Find each parasitized RBC.
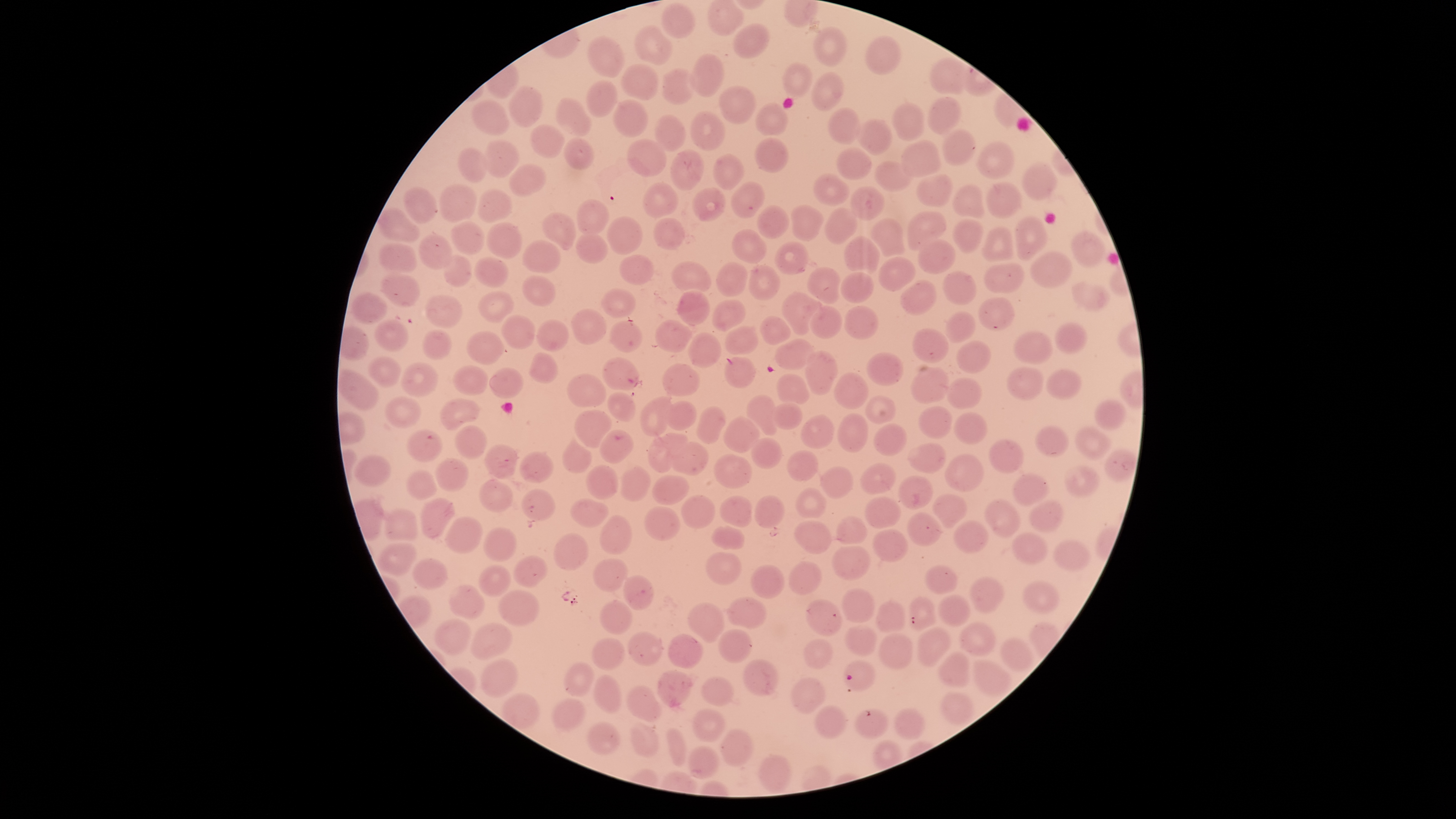

Approximate bounding boxes as {left, top, right, bottom} in pixels.
Parasitized RBCs: {843, 661, 877, 690}.

Approximate bounding boxes as {left, top, right, bottom} in pixels.
Summary:
  - Uninfected RBCs: {707, 0, 746, 36}, {661, 4, 697, 38}, {733, 23, 770, 58}, {634, 26, 673, 65}, {813, 27, 848, 66}, {865, 35, 901, 76}, {588, 37, 624, 78}, {690, 53, 725, 96}, {929, 56, 969, 95}, {783, 62, 813, 97}, {620, 63, 658, 100}, {662, 68, 694, 105}, {812, 73, 845, 111}, {586, 81, 618, 118}, {509, 86, 545, 128}, {718, 86, 756, 125}, {927, 97, 962, 134}, {555, 98, 591, 135}, {613, 100, 648, 137}, {470, 102, 509, 135}, {891, 103, 924, 141}, {755, 104, 790, 136}, {828, 107, 860, 145}, {689, 110, 726, 151}, {655, 115, 686, 150}, {858, 119, 892, 156}, {530, 124, 564, 159}, {941, 129, 976, 166}, {564, 138, 593, 169}, {627, 138, 666, 177}, {754, 138, 787, 173}, {484, 140, 519, 177}, {901, 140, 941, 177}, {977, 142, 1014, 178}, {836, 147, 872, 180}, {458, 148, 489, 183}, {671, 149, 704, 191}, {713, 153, 743, 192}, {875, 160, 914, 191}, {510, 163, 545, 197}, {1022, 164, 1058, 200}, {813, 173, 850, 208}, {917, 174, 953, 207}, {643, 182, 679, 217}, {731, 182, 765, 219}, {986, 182, 1023, 219}, {440, 184, 477, 223}, {952, 184, 985, 219}, {849, 186, 886, 220}, {403, 187, 438, 223}, {692, 188, 726, 221}, {477, 189, 513, 223}, {577, 198, 608, 236}, {758, 204, 789, 238}, {792, 205, 824, 242}, {824, 206, 858, 242}, {378, 208, 419, 242}, {907, 212, 948, 250}, {541, 214, 576, 250}, {606, 216, 643, 256}, {1015, 216, 1049, 261}, {871, 217, 904, 256}, {653, 218, 687, 249}, {951, 220, 984, 253}, {451, 222, 485, 255}, {487, 223, 521, 258}, {979, 226, 1013, 262}, {730, 228, 766, 262}, {1070, 229, 1104, 267}, {576, 232, 607, 264}, {419, 235, 453, 269}, {842, 236, 881, 274}, {916, 238, 956, 277}, {522, 239, 560, 274}, {773, 241, 809, 274}, {380, 243, 417, 272}, {1030, 251, 1072, 289}, {618, 253, 655, 285}, {443, 256, 471, 288}, {474, 257, 510, 287}, {878, 257, 915, 292}, {671, 261, 712, 293}, {714, 263, 748, 297}, {749, 264, 780, 300}, {983, 264, 1024, 293}, {807, 267, 840, 303}, {942, 271, 976, 305}, {839, 272, 875, 303}, {382, 274, 419, 308}, {522, 276, 557, 306}, {900, 280, 936, 314}, {1072, 281, 1111, 310}, {600, 288, 636, 318}, {677, 288, 710, 326}, {478, 291, 514, 323}, {352, 292, 387, 324}, {782, 292, 823, 335}, {426, 295, 463, 329}, {978, 297, 1014, 332}, {711, 299, 747, 332}, {809, 306, 841, 340}, {844, 306, 879, 339}, {571, 309, 608, 344}, {945, 311, 976, 341}, {502, 314, 535, 348}, {759, 316, 791, 344}, {375, 318, 409, 353}, {537, 320, 569, 351}, {654, 320, 693, 354}, {609, 321, 643, 352}, {1054, 322, 1086, 353}, {724, 326, 759, 356}, {422, 329, 453, 361}, {911, 329, 948, 363}, {465, 331, 504, 366}, {1014, 331, 1052, 365}, {687, 332, 722, 368}, {774, 338, 816, 370}, {957, 340, 990, 373}, {804, 351, 838, 393}, {868, 351, 902, 386}, {530, 353, 558, 384}, {724, 356, 756, 389}, {368, 357, 404, 387}, {602, 357, 640, 390}, {662, 363, 699, 397}, {400, 364, 439, 397}, {453, 366, 488, 396}, {910, 366, 948, 403}, {490, 368, 525, 399}, {1006, 368, 1044, 400}, {1046, 369, 1081, 399}, {338, 370, 378, 412}, {835, 372, 869, 409}, {775, 374, 812, 405}, {565, 375, 607, 407}, {946, 376, 981, 409}, {606, 393, 635, 423}, {746, 394, 781, 436}, {865, 395, 895, 424}, {386, 396, 422, 429}, {639, 396, 675, 438}, {441, 400, 479, 431}, {666, 400, 697, 430}, {772, 401, 803, 430}, {1094, 401, 1126, 431}, {696, 405, 725, 444}, {917, 406, 952, 439}, {573, 409, 612, 449}, {954, 412, 988, 445}, {838, 414, 868, 452}, {799, 415, 834, 449}, {723, 416, 759, 452}, {874, 424, 907, 456}, {455, 426, 487, 459}, {1035, 426, 1069, 457}, {1074, 427, 1113, 459}, {599, 429, 632, 463}, {405, 430, 443, 462}, {646, 434, 689, 473}, {562, 438, 591, 473}, {750, 438, 783, 469}, {989, 439, 1023, 473}, {670, 442, 709, 476}, {908, 442, 947, 473}, {485, 445, 518, 478}, {787, 450, 817, 481}, {1105, 450, 1136, 482}, {520, 453, 555, 484}, {713, 453, 753, 489}, {353, 455, 391, 487}, {944, 455, 984, 492}, {434, 457, 469, 491}, {860, 463, 895, 495}, {620, 464, 652, 501}, {585, 465, 618, 500}, {820, 467, 852, 499}, {1063, 467, 1101, 497}, {406, 471, 438, 500}, {1011, 472, 1050, 507}, {652, 475, 689, 505}, {898, 476, 933, 508}, {480, 480, 514, 513}, {522, 488, 555, 522}, {796, 488, 827, 519}, {680, 495, 716, 529}, {720, 495, 752, 527}, {933, 495, 967, 528}, {755, 496, 785, 529}, {865, 497, 901, 528}, {421, 499, 455, 539}, {570, 500, 608, 528}, {986, 501, 1023, 539}, {1030, 503, 1063, 533}, {644, 506, 681, 541}, {383, 509, 418, 541}, {906, 512, 942, 546}, {598, 514, 632, 556}, {836, 515, 868, 546}, {446, 517, 484, 553}, {794, 521, 833, 554}, {953, 521, 989, 554}, {711, 526, 745, 550}, {483, 528, 518, 562}, {874, 529, 908, 562}, {1012, 531, 1048, 564}, {554, 533, 589, 571}, {1052, 541, 1090, 571}, {378, 543, 416, 578}, {833, 546, 870, 581}, {705, 551, 742, 586}, {514, 556, 547, 588}, {411, 559, 448, 591}, {593, 559, 628, 591}, {789, 561, 822, 594}, {923, 563, 957, 595}, {477, 564, 511, 597}, {751, 564, 784, 600}, {624, 574, 654, 610}, {969, 576, 1005, 613}, {1024, 582, 1060, 614}, {448, 586, 486, 620}, {496, 589, 541, 626}, {842, 589, 876, 624}, {939, 594, 971, 628}, {728, 597, 767, 628}, {806, 599, 842, 636}, {909, 599, 937, 631}, {601, 601, 632, 635}, {877, 601, 904, 633}, {688, 602, 724, 642}, {433, 620, 471, 655}, {959, 624, 996, 658}, {471, 625, 514, 661}, {718, 627, 752, 663}, {844, 627, 877, 656}, {918, 627, 953, 666}, {628, 631, 663, 667}, {878, 633, 914, 670}, {668, 634, 703, 669}, {592, 637, 624, 671}, {1000, 638, 1033, 673}, {804, 639, 833, 668}, {938, 653, 970, 687}, {744, 659, 778, 695}, {481, 660, 518, 698}, {974, 661, 1011, 696}, {565, 663, 595, 697}, {657, 671, 692, 706}, {593, 675, 623, 713}, {792, 677, 825, 713}, {702, 678, 734, 706}, {626, 687, 662, 722}, {941, 692, 973, 726}, {501, 694, 540, 729}, {554, 700, 583, 731}, {815, 706, 847, 740}, {895, 707, 925, 740}, {691, 709, 725, 742}, {855, 709, 889, 739}, {588, 721, 622, 757}, {631, 721, 659, 757}, {722, 730, 754, 767}, {666, 731, 687, 767}, {687, 744, 720, 780}, {757, 752, 792, 794}
  - Visible region: circular
  - Capture: smartphone photograph through the microscope eyepiece
  - Field of view: single
  - Preparation: thin blood smear
  - Image size: 1456×819 pixels
  - Species: Plasmodium falciparum
  - Stain: Giemsa